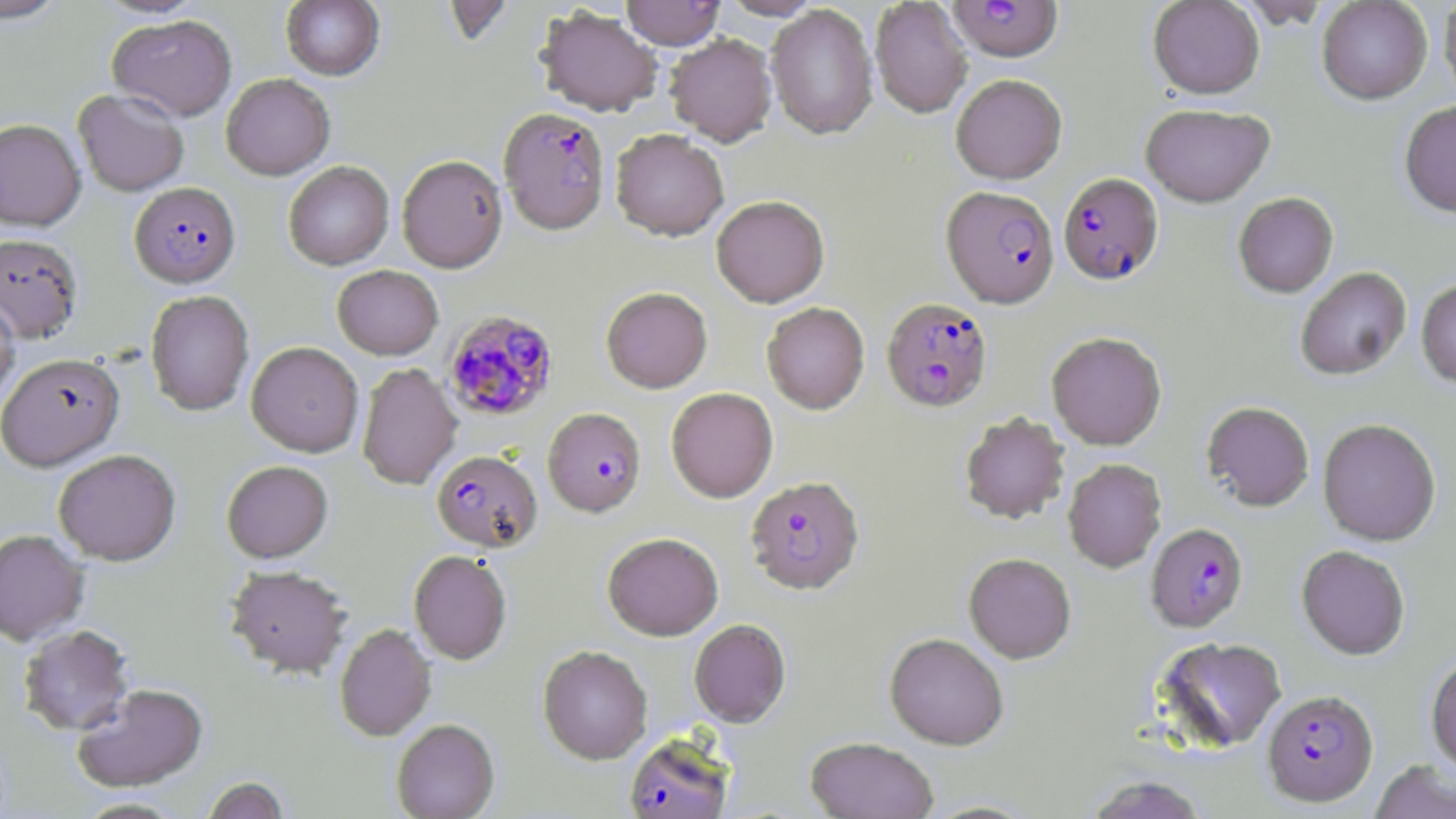

{
  "slide_level_diagnosis": "Plasmodium falciparum",
  "image_size": "1456×819 pixels",
  "preparation": "thin blood smear",
  "plasmodium_falciparum_infected_red_blood_cell_locations": "approximate bounding boxes as [x1, y1, x2, y2] in pixels: [947, 0, 1063, 60], [499, 107, 610, 235], [1059, 173, 1163, 285], [129, 182, 240, 287], [942, 186, 1059, 307], [881, 297, 993, 412], [443, 309, 559, 422], [543, 407, 646, 516], [431, 450, 542, 552], [746, 476, 864, 595], [1147, 523, 1248, 632], [1263, 689, 1378, 807], [623, 733, 734, 819]",
  "uninfected_red_blood_cell_locations": "approximate bounding boxes as [x1, y1, x2, y2] in pixels: [0, 0, 71, 24], [621, 0, 725, 49], [719, 0, 822, 20], [870, 0, 972, 118], [1148, 0, 1265, 99], [1234, 0, 1334, 28], [1317, 0, 1432, 104], [1439, 0, 1456, 104], [281, 1, 384, 80], [441, 1, 515, 46], [767, 4, 878, 140], [536, 6, 662, 116], [107, 14, 237, 121], [665, 34, 777, 147], [221, 73, 334, 179], [951, 74, 1067, 184], [73, 88, 189, 196], [1399, 101, 1456, 218], [1140, 103, 1275, 206], [0, 118, 86, 230], [611, 129, 729, 240], [397, 154, 508, 272], [283, 161, 394, 269], [1233, 192, 1338, 297], [711, 195, 829, 307], [0, 232, 83, 344], [332, 265, 443, 359], [1295, 266, 1411, 380], [1416, 279, 1456, 387], [601, 287, 712, 393], [146, 290, 254, 416], [0, 294, 20, 411], [762, 302, 869, 414], [1046, 332, 1167, 450], [246, 341, 364, 456], [0, 352, 124, 470], [357, 362, 462, 490], [666, 387, 778, 502], [1202, 401, 1315, 511], [960, 412, 1070, 524], [1318, 418, 1441, 545], [53, 448, 181, 565], [1063, 458, 1166, 572], [222, 460, 333, 562], [0, 529, 89, 645], [603, 532, 723, 640], [1296, 545, 1410, 660], [409, 550, 512, 664], [964, 553, 1076, 663], [226, 565, 353, 677], [689, 619, 791, 727], [334, 623, 436, 741], [18, 624, 135, 736], [885, 633, 1008, 750], [1154, 637, 1287, 752], [538, 645, 652, 764], [1426, 654, 1456, 776], [72, 683, 209, 792], [391, 718, 500, 818], [805, 737, 939, 819], [1370, 761, 1456, 819], [1083, 774, 1210, 818], [200, 776, 291, 819], [74, 797, 187, 818], [919, 798, 1042, 818]",
  "field_of_view": "one of a larger specimen",
  "stain": "May-Grünwald-Giemsa",
  "magnification": "1000x",
  "modality": "optical microscopy"
}